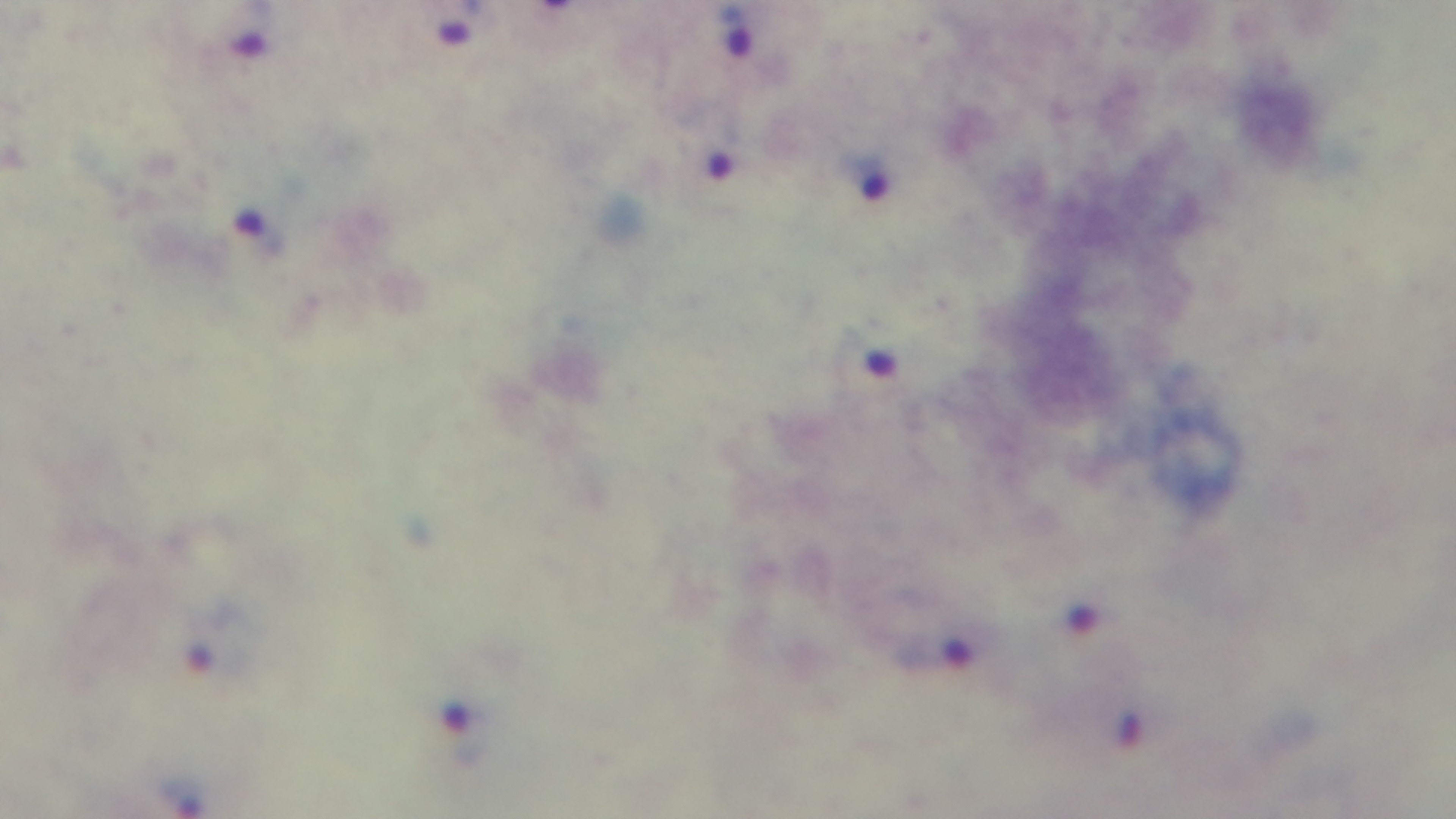

{
  "stain": "Giemsa",
  "modality": "light microscopy",
  "malaria_status": "positive",
  "capture": "mounted 4K digital camera",
  "objective": "100x oil immersion",
  "field_of_view": "single",
  "preparation": "thick smear"
}